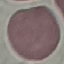

Summary:
  - Malaria status: uninfected
  - Image type: automatically extracted cell patch, resized to 64 × 64 pixels
  - Preparation: thin blood film
  - Capture: smartphone camera at the microscope eyepiece
  - Stain: Giemsa